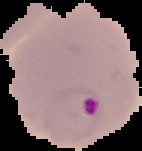

image type = segmented cell region on a black background
preparation = thin blood smear
result = Plasmodium parasites identified
image size = 142×151 pixels